Locate every blood parasite and identify its species.
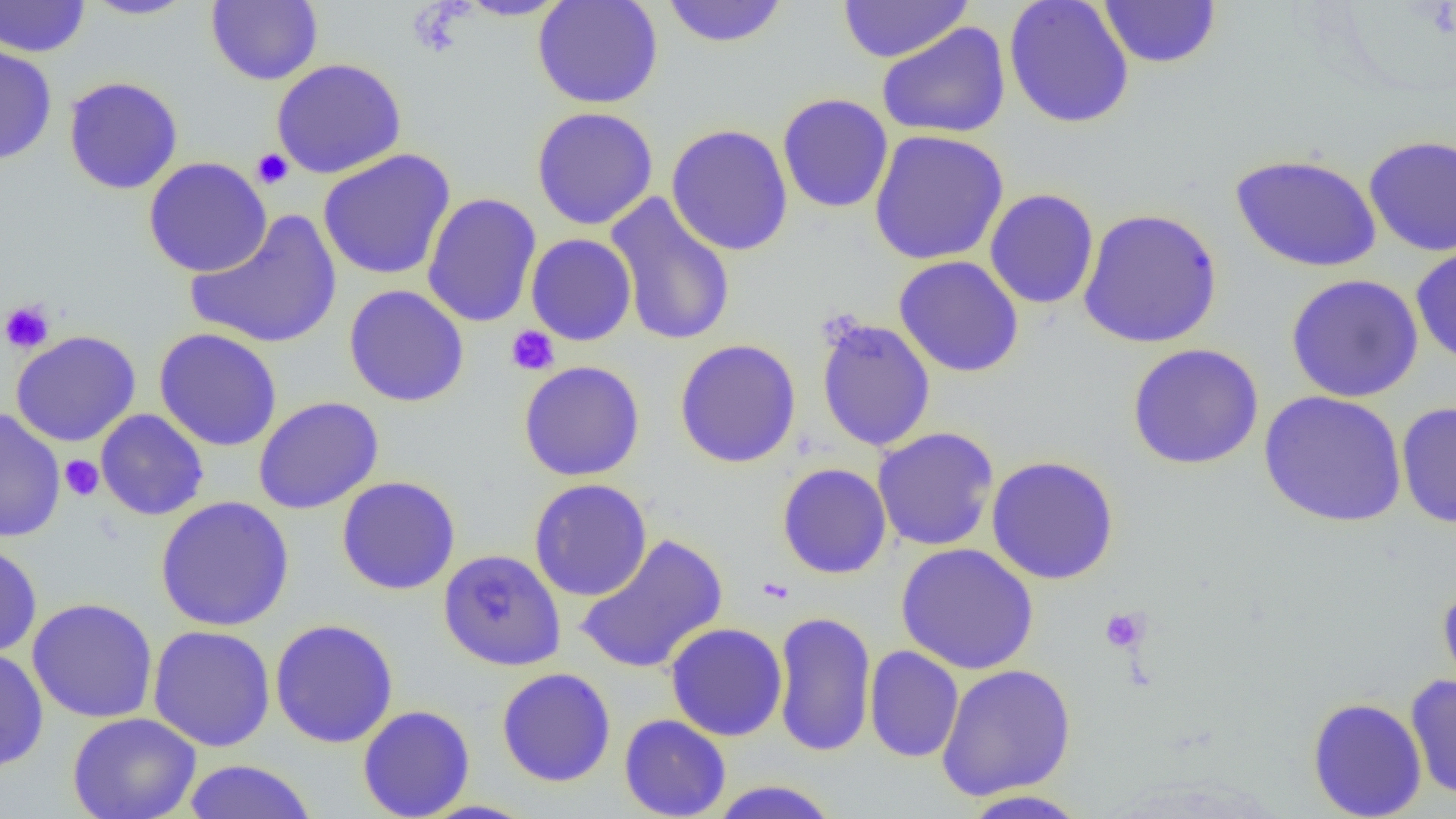

No blood parasites observed.

slide_level_diagnosis: no evidence of blood parasites
field_of_view: single
magnification: 1000x
preparation: thin blood film
uninfected_red_blood_cell_locations: 'approximate bounding boxes as [x1, y1, x2, y2] in pixels: [0, 0, 90, 57], [79, 0, 197, 20], [454, 0, 573, 21], [532, 0, 664, 109], [838, 0, 972, 63], [1004, 0, 1134, 128], [1097, 0, 1222, 69], [206, 1, 323, 85], [661, 1, 789, 48], [876, 21, 1011, 139], [0, 41, 57, 166], [270, 58, 407, 179], [63, 76, 183, 194], [777, 93, 893, 214], [531, 106, 659, 230], [666, 123, 794, 256], [868, 129, 1009, 266], [1362, 134, 1456, 257], [317, 149, 456, 281], [1230, 153, 1382, 273], [143, 157, 272, 277], [984, 188, 1099, 309], [422, 192, 541, 328], [604, 192, 737, 347], [1078, 208, 1223, 348], [185, 210, 342, 349], [525, 233, 637, 346], [1410, 243, 1456, 367], [893, 256, 1024, 378], [1285, 273, 1424, 403], [343, 285, 470, 407], [815, 316, 937, 452], [154, 328, 283, 452], [11, 330, 141, 447], [674, 338, 802, 468], [1127, 343, 1264, 469], [518, 360, 646, 481], [1259, 391, 1407, 527], [253, 396, 384, 514], [1396, 400, 1456, 529], [0, 407, 66, 543], [95, 409, 209, 521], [872, 427, 999, 551], [986, 455, 1119, 584], [777, 463, 892, 579], [337, 476, 460, 595], [528, 478, 652, 601], [154, 496, 295, 632], [574, 533, 728, 675], [0, 542, 42, 657], [896, 542, 1039, 674], [438, 549, 566, 671], [1437, 579, 1456, 702], [27, 597, 159, 723], [772, 610, 877, 758], [269, 617, 399, 748], [666, 622, 787, 741], [147, 624, 276, 752], [864, 645, 964, 763], [0, 647, 48, 773], [936, 663, 1076, 801], [496, 667, 616, 786], [1404, 674, 1456, 799], [1307, 696, 1428, 819], [358, 704, 475, 819], [67, 712, 202, 819], [619, 714, 731, 819], [182, 759, 317, 819], [708, 779, 841, 818], [958, 790, 1090, 818]'
platelet_locations: 'approximate bounding boxes as [x1, y1, x2, y2] in pixels: [251, 148, 294, 189], [0, 300, 56, 354], [505, 325, 560, 376], [59, 456, 104, 501], [1100, 607, 1149, 653]'
modality: light microscopy
image_size: 1456×819 pixels